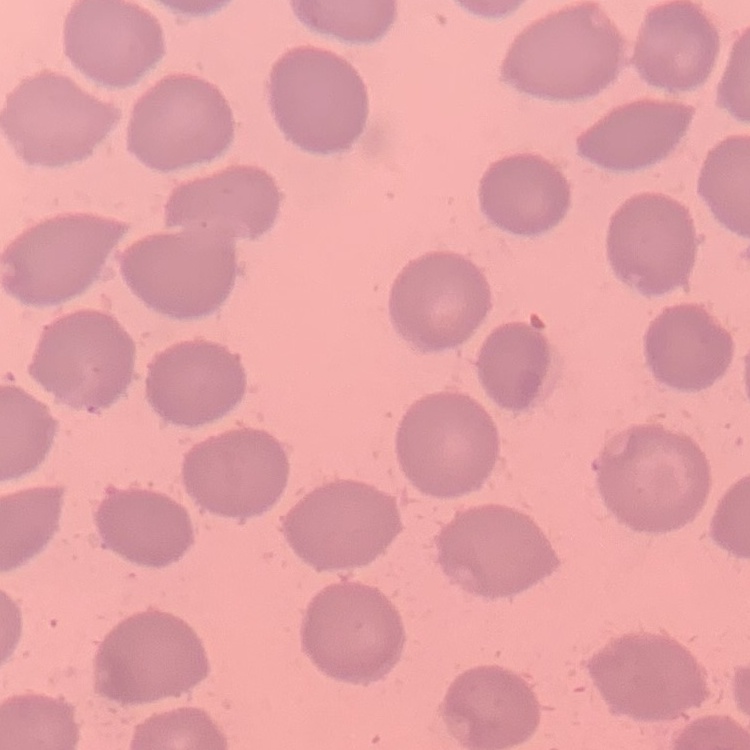

erythrocyte morphology = no rouleaux formation
image type = one tile cut from a larger photomicrograph
preparation = thin blood smear
stain = Field's or Giemsa